Comment on the morphology of the erythrocytes.
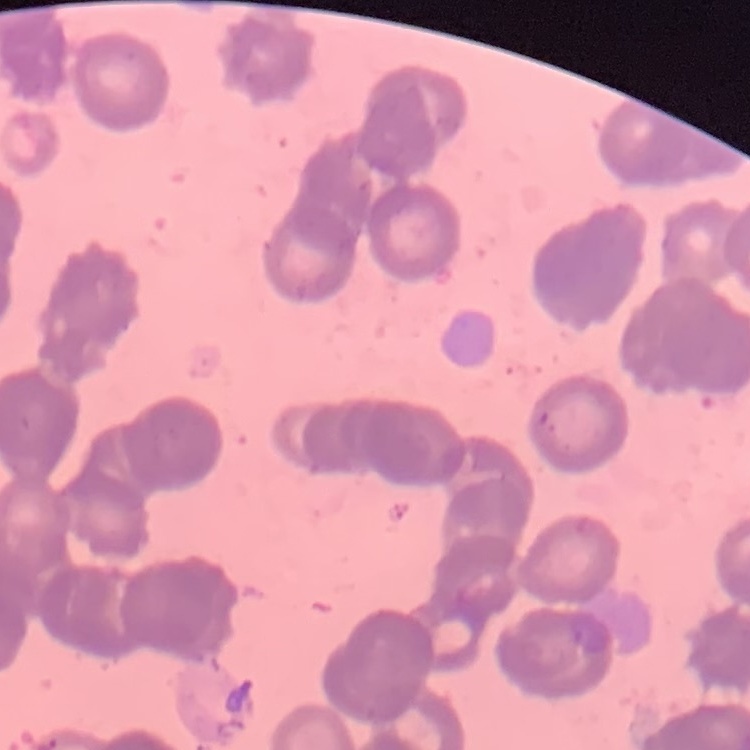
They show rouleaux formation.

Stained with either Field's or Giemsa. Thin blood smear. One tile cut from a larger photomicrograph.